Assess this cell for malaria.
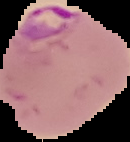

It is parasitized.

{
  "image_size": "130×142 pixels",
  "image_type": "cell region segmented out of the field of view; surrounding area masked to black",
  "preparation": "thin blood film"
}